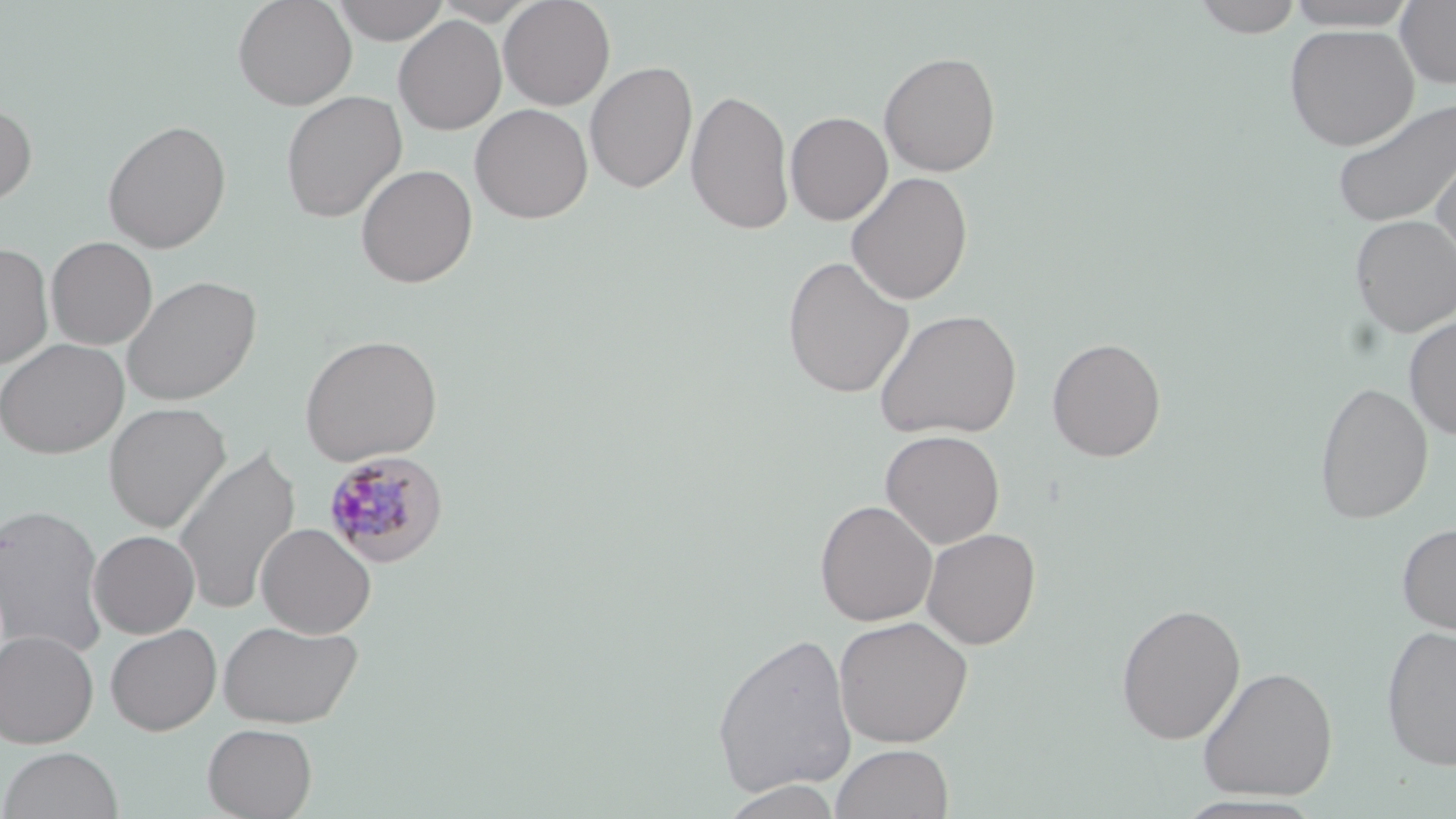 Approximate bounding boxes as (x1,y1)-(x2,y2) corner pairs in pixels. Plasmodium malariae-infected red blood cell locations: (322,451)-(448,568). Uninfected red blood cell locations: (232,0)-(357,110), (332,0)-(449,44), (499,0)-(616,110), (1192,0)-(1304,38), (1282,0)-(1421,30), (1395,1)-(1456,89), (393,15)-(506,135), (1283,24)-(1419,150), (879,50)-(1001,177), (585,61)-(698,194), (686,88)-(795,235), (280,90)-(407,223), (1330,95)-(1455,228), (0,101)-(37,207), (470,103)-(593,223), (785,111)-(892,225), (102,119)-(232,253), (1430,138)-(1456,268), (356,163)-(477,288), (846,172)-(973,305), (1350,215)-(1456,337), (46,236)-(157,350), (0,243)-(54,368), (782,255)-(915,398), (121,274)-(261,406), (873,308)-(1022,440), (1403,316)-(1456,439), (299,334)-(443,466), (1046,336)-(1166,462), (0,338)-(128,459), (1314,380)-(1433,524), (104,402)-(231,533), (880,429)-(1005,549), (172,443)-(301,616), (815,500)-(938,627), (1,503)-(109,658), (1396,521)-(1456,635), (256,523)-(376,638), (921,527)-(1041,649), (89,530)-(200,638), (1115,602)-(1246,744), (833,615)-(974,748), (217,619)-(364,730), (105,623)-(221,735), (1381,625)-(1456,771), (1,629)-(99,747), (711,629)-(858,800), (1197,666)-(1338,801), (202,723)-(318,819), (830,743)-(954,819), (0,746)-(123,819), (719,780)-(844,819), (1170,794)-(1326,818). Slide-level diagnosis: Plasmodium malariae. Thin blood smear. One field of a larger specimen. Light microscopy. Captured at 1000x magnification. Image is 1456×819 pixels. May-Grünwald-Giemsa-stained preparation.